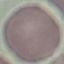
Summary:
  - Malaria status: uninfected
  - Capture: smartphone camera at the microscope eyepiece
  - Image type: automatically extracted cell patch, resized to 64 × 64 pixels
  - Stain: Giemsa
  - Preparation: thin smear